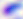

Toxoplasma gondii is shown. Micrograph. 400x magnification.